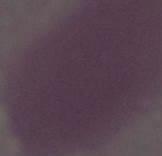
Summary:
  - Modality: photomicrograph
  - Identification: erythrocyte
  - Magnification: 1000x